State which parasite is depicted.
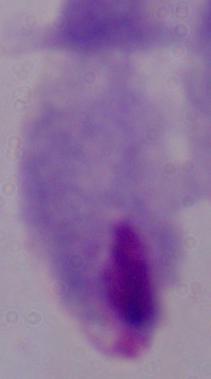
This is a trichomonad.

Photomicrograph. 1000x magnification.